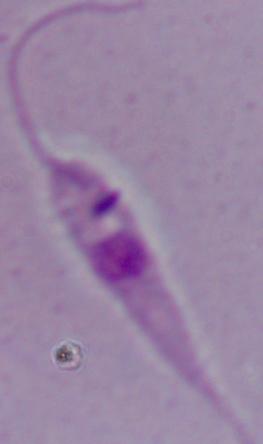
1000x magnification. A Leishmania parasite is seen. Photomicrograph.